Point out every Plasmodium parasite.
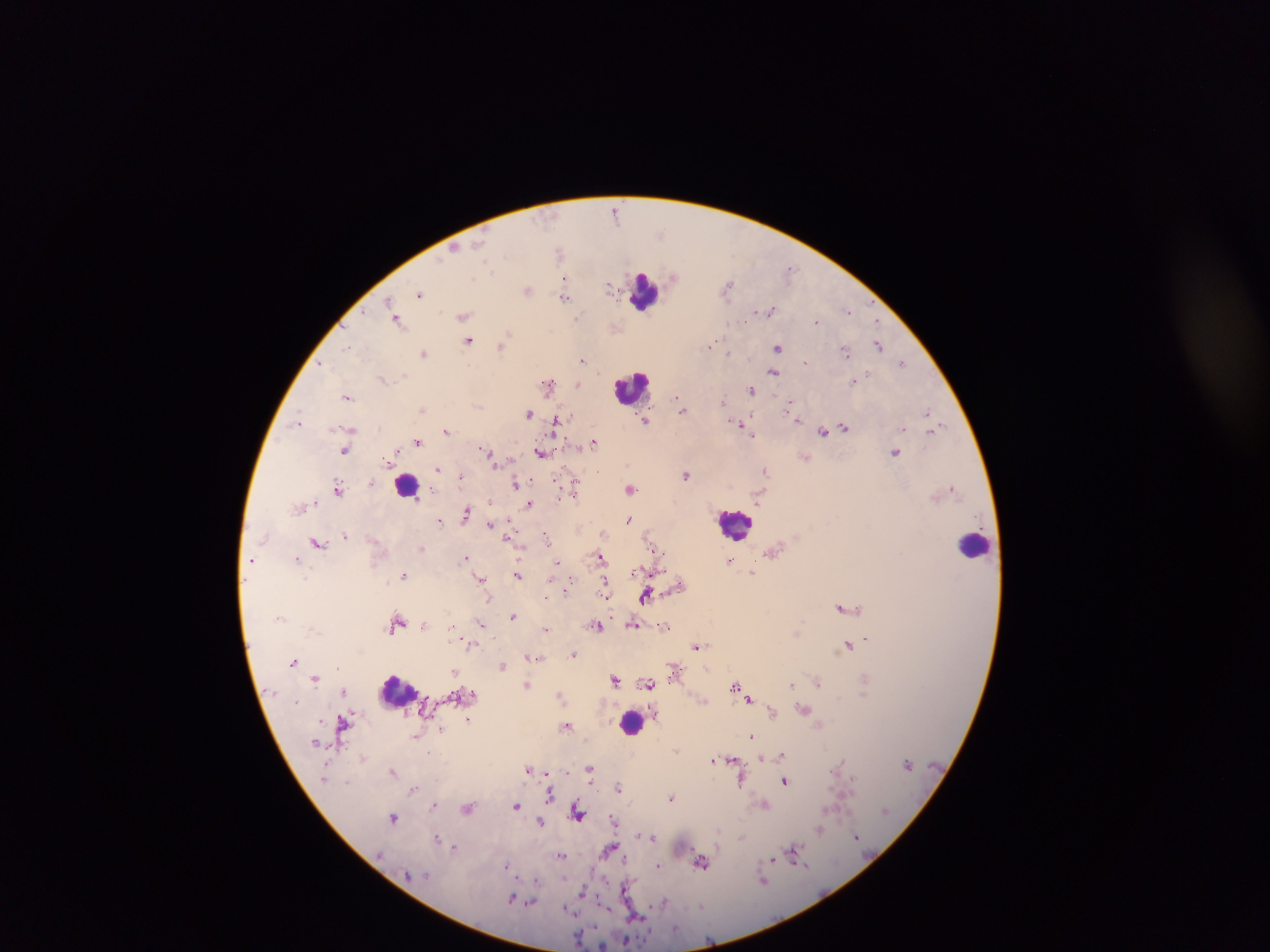
Approximate centers as x y in pixels.
Plasmodium parasites: 615 212; 660 234; 455 248; 558 251; 789 269; 674 277; 474 278; 565 278; 609 286; 728 288; 528 290; 420 294; 565 296; 388 302; 771 310; 848 310; 463 316; 577 319; 397 320; 817 320; 468 341; 709 345; 879 345; 348 346; 501 346; 777 347; 728 352; 846 352; 424 353; 582 360; 805 362; 903 362; 323 364; 773 372; 382 378; 853 381; 578 384; 548 385; 751 389; 347 397; 678 399; 724 400; 681 407; 790 407; 422 409; 928 413; 529 414; 794 414; 798 420; 300 421; 646 421; 555 424; 737 424; 844 426; 933 429; 446 430; 824 432; 752 434; 418 442; 594 442; 345 450; 541 452; 895 452; 490 455; 805 458; 438 470; 765 471; 686 474; 461 477; 515 482; 371 483; 338 488; 953 488; 631 489; 575 490; 758 500; 314 502; 530 504; 467 514; 629 519; 440 521; 509 522; 489 524; 603 534; 345 536; 547 537; 318 542; 658 551; 773 552; 465 558; 602 558; 252 559; 296 559; 729 561; 557 562; 752 573; 517 574; 404 576; 482 579; 572 581; 604 581; 607 586; 645 595; 546 597; 843 607; 513 616; 397 623; 481 623; 633 624; 424 625; 452 625; 597 626; 545 628; 866 639; 848 645; 697 646; 471 647; 573 654; 532 658; 538 658; 294 662; 503 666; 455 671; 674 673; 314 678; 615 679; 818 682; 649 684; 527 685; 792 685; 735 687; 344 691; 472 694; 560 696; 749 699; 805 709; 772 712; 656 713; 468 720; 343 722; 567 726; 442 729; 416 736; 751 736; 315 743; 677 750; 782 755; 363 759; 761 759; 714 760; 732 760; 841 760; 589 768; 529 769; 394 773; 546 773; 590 776; 853 781; 742 782; 785 782; 619 788; 413 790; 550 796; 671 797; 434 804; 516 806; 766 806; 468 808; 578 812; 393 817; 614 820; 540 822; 820 829; 857 836; 652 837; 742 837; 437 838; 454 847; 609 850; 795 850; 561 855; 773 859; 625 860; 702 863; 507 865; 658 865; 583 894; 512 899; 664 900; 531 902; 578 939; 625 941.

Summary:
  - Leukocyte locations (subset; some below the resolvable size): 645 293; 632 387; 405 486; 735 524; 974 545; 397 693; 631 722
  - Capture: mobile-phone photograph through a microscope
  - Image size: 1270×952 pixels
  - Preparation: thick blood film
  - Country: Ghana
  - Field of view: single